Assess the morphology of the red blood cells.
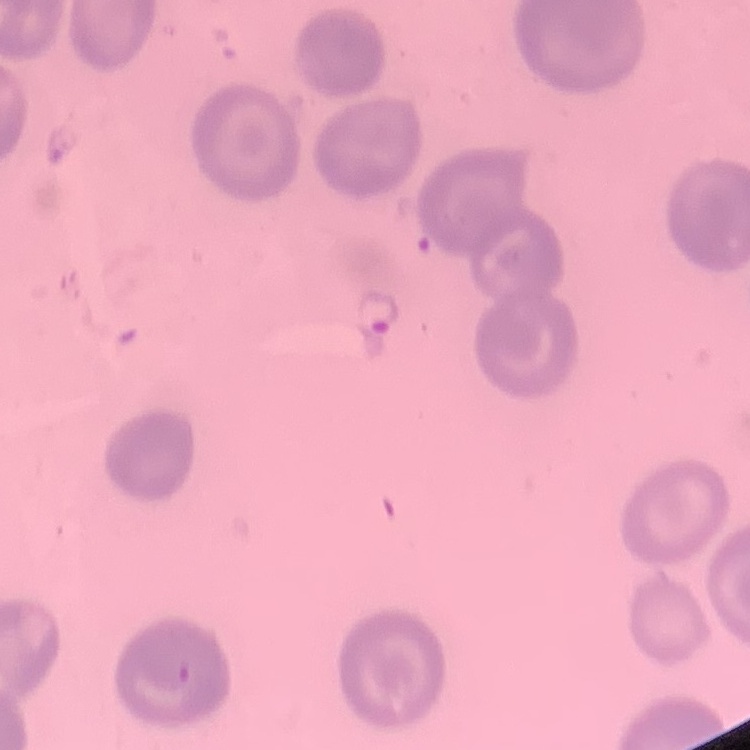

No rouleaux formation.

image type = one tile cut from a larger photomicrograph
stain = Field's or Giemsa
preparation = thin blood smear